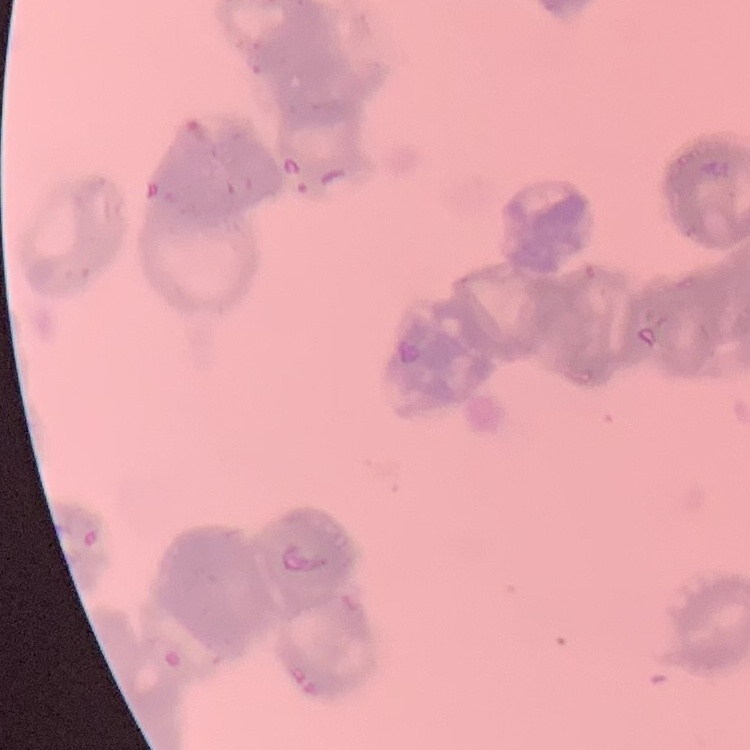

red blood cell morphology = rouleaux formation
image type = one tile cut from a larger photomicrograph
stain = Field's or Giemsa
preparation = thin peripheral smear